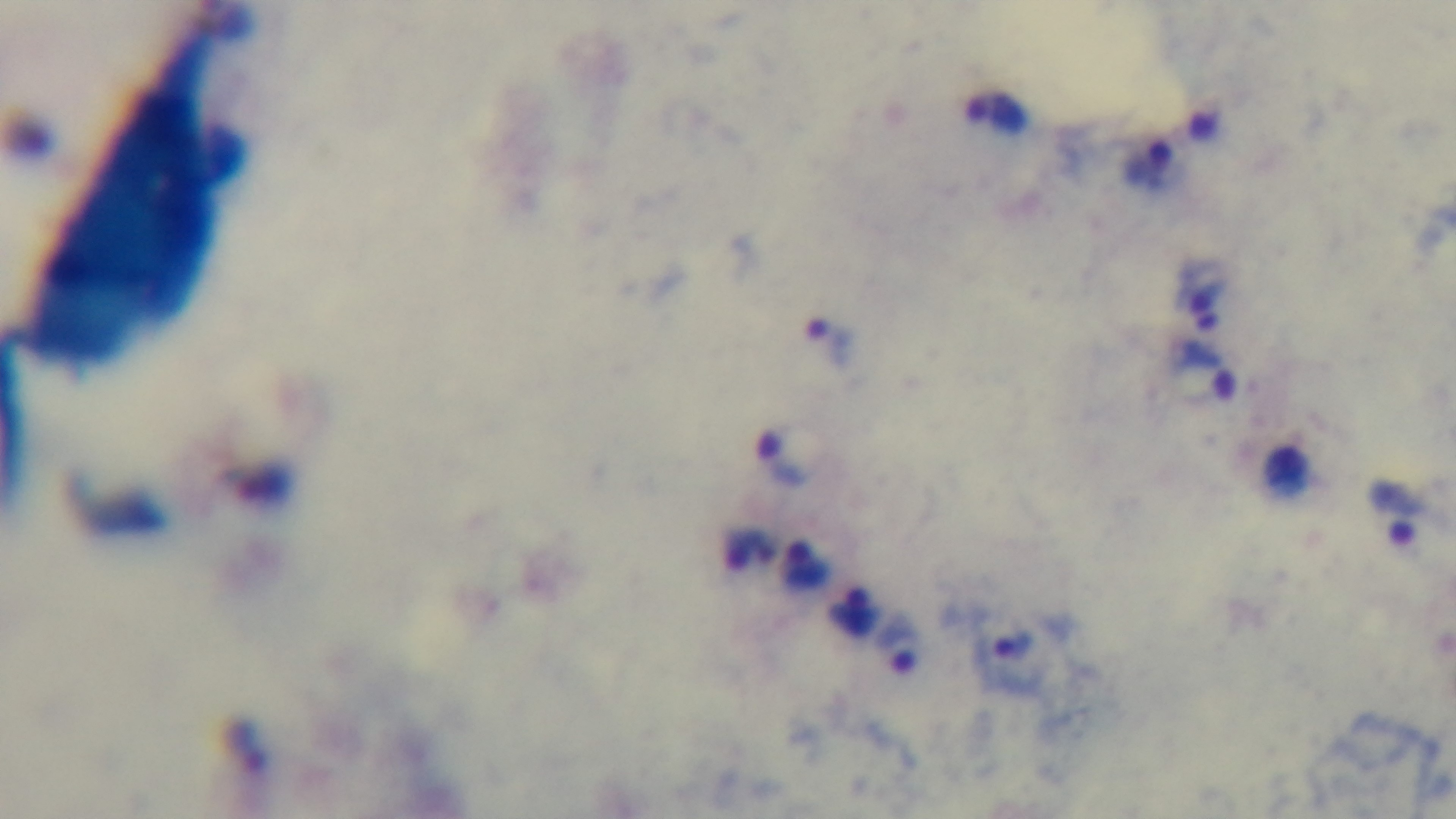

capture = mounted 4K digital camera
preparation = thick blood film
objective = 100x oil immersion
field of view = one from the slide
modality = light microscopy
stain = Giemsa
malaria status = infected